Locate every blood parasite and identify its species.
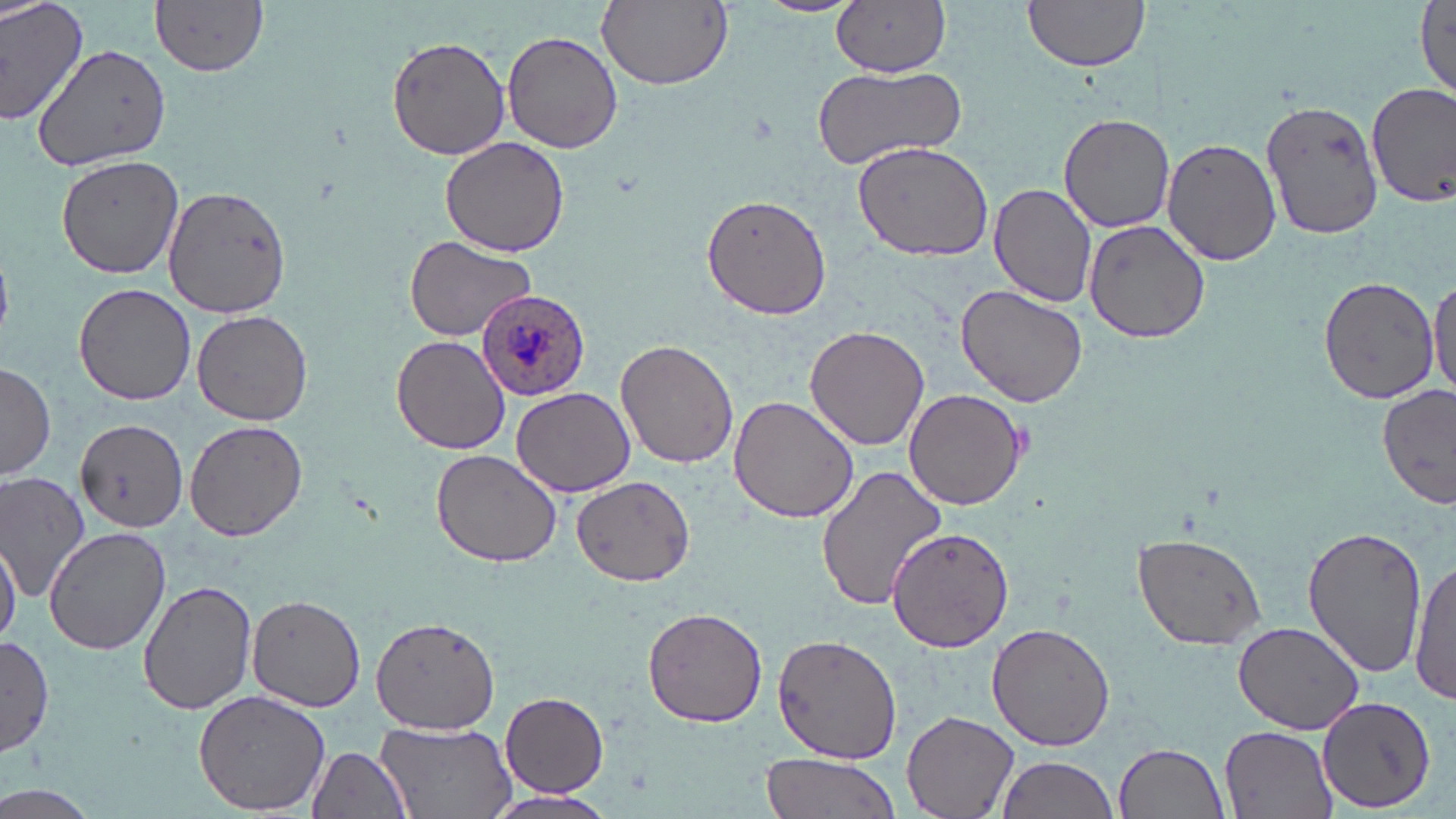
Approximate bounding boxes as (x1,y1)-(x2,y2) corner pairs in pixels.
Plasmodium ovale-infected red blood cells: (476,290)-(593,402).
No Plasmodium falciparum, Plasmodium malariae, Plasmodium vivax, Babesia divergens, or Trypanosoma brucei observed.

Summary:
  - Uninfected red blood cell locations: (0,0)-(91,127), (826,0)-(949,79), (1021,0)-(1151,73), (152,1)-(270,76), (596,1)-(733,89), (1415,2)-(1454,104), (501,30)-(623,153), (387,33)-(511,160), (31,43)-(175,173), (812,65)-(966,170), (1369,84)-(1456,209), (1261,100)-(1388,241), (1058,112)-(1175,232), (439,136)-(570,257), (851,137)-(996,261), (1161,137)-(1283,265), (57,153)-(185,280), (989,182)-(1098,308), (162,184)-(294,320), (701,191)-(832,319), (1082,216)-(1213,343), (404,236)-(535,342), (1428,270)-(1455,402), (1317,276)-(1439,402), (73,282)-(196,406), (955,286)-(1089,408), (190,308)-(313,425), (805,324)-(929,450), (391,335)-(511,455), (617,340)-(740,470), (0,361)-(55,482), (1378,383)-(1455,509), (511,386)-(635,497), (904,388)-(1027,510), (729,394)-(859,523), (72,411)-(189,536), (184,421)-(307,541), (431,450)-(561,568), (814,463)-(949,611), (0,472)-(93,597), (571,474)-(694,586), (886,525)-(1017,652), (1301,525)-(1427,678), (42,527)-(170,656), (1132,533)-(1269,650), (0,538)-(20,644), (1411,555)-(1455,706), (138,578)-(257,716), (246,593)-(365,713), (642,605)-(768,727), (371,615)-(500,735), (1232,618)-(1364,733), (986,623)-(1115,752), (0,634)-(55,756), (770,634)-(902,765), (193,689)-(333,815), (498,691)-(611,798), (1317,695)-(1436,813), (900,711)-(1019,819), (373,720)-(516,819), (1220,726)-(1336,819), (1114,742)-(1229,819), (307,744)-(415,819), (759,751)-(901,819), (994,756)-(1119,819), (480,790)-(617,819)
  - Slide-level diagnosis: Plasmodium ovale
  - Preparation: thin blood smear
  - Stain: May-Grünwald-Giemsa
  - Magnification: 1000x
  - Image size: 1456×819 pixels
  - Modality: light microscopy
  - Field of view: one of a larger specimen